Classify this cell by malaria status.
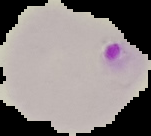
It is parasitized.

Summary:
  - Image size: 151×136 pixels
  - Preparation: thin blood smear
  - Image type: cell region segmented out of the field of view; surrounding area masked to black